State which parasite is depicted.
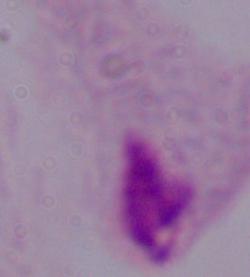

A trichomonad.

magnification = 1000x
modality = micrograph